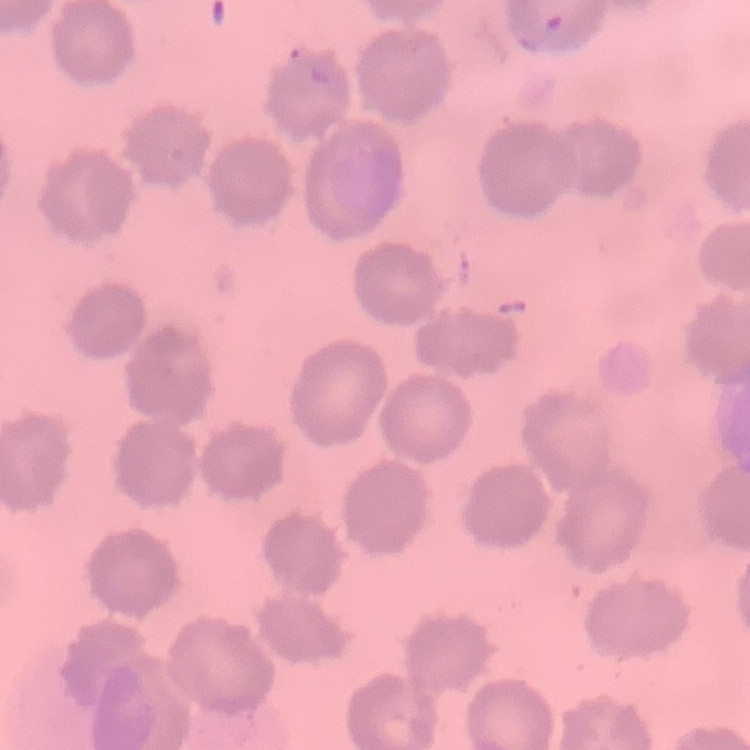
Summary:
  - Red blood cell morphology: no rouleaux formation
  - Preparation: thin peripheral smear
  - Image type: square crop of a larger photomicrograph
  - Stain: Field's or Giemsa